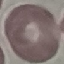 Malaria status: uninfected. Giemsa stain. Photographed with a smartphone camera at the microscope eyepiece. Cell patch, automatically extracted from a larger field of view and resized to 64 × 64 pixels. Thin smear of blood.